Name the parasite shown.
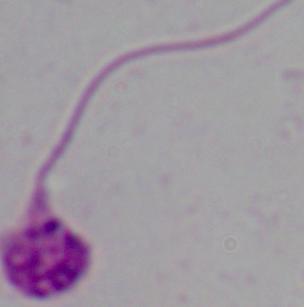

Leishmania.

Summary:
  - Modality: micrograph
  - Magnification: 1000x